Report the malaria status of this cell.
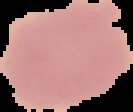

It is uninfected.

Summary:
  - Image size: 133×112 pixels
  - Preparation: thin blood film
  - Image type: cell region segmented out of the field of view; surrounding area masked to black